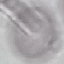

{
  "malaria_status": "uninfected",
  "stain": "Giemsa",
  "preparation": "thin blood smear",
  "image_type": "cell patch, automatically extracted from a larger field of view and resized to 64 × 64 pixels",
  "capture": "smartphone through the microscope eyepiece"
}